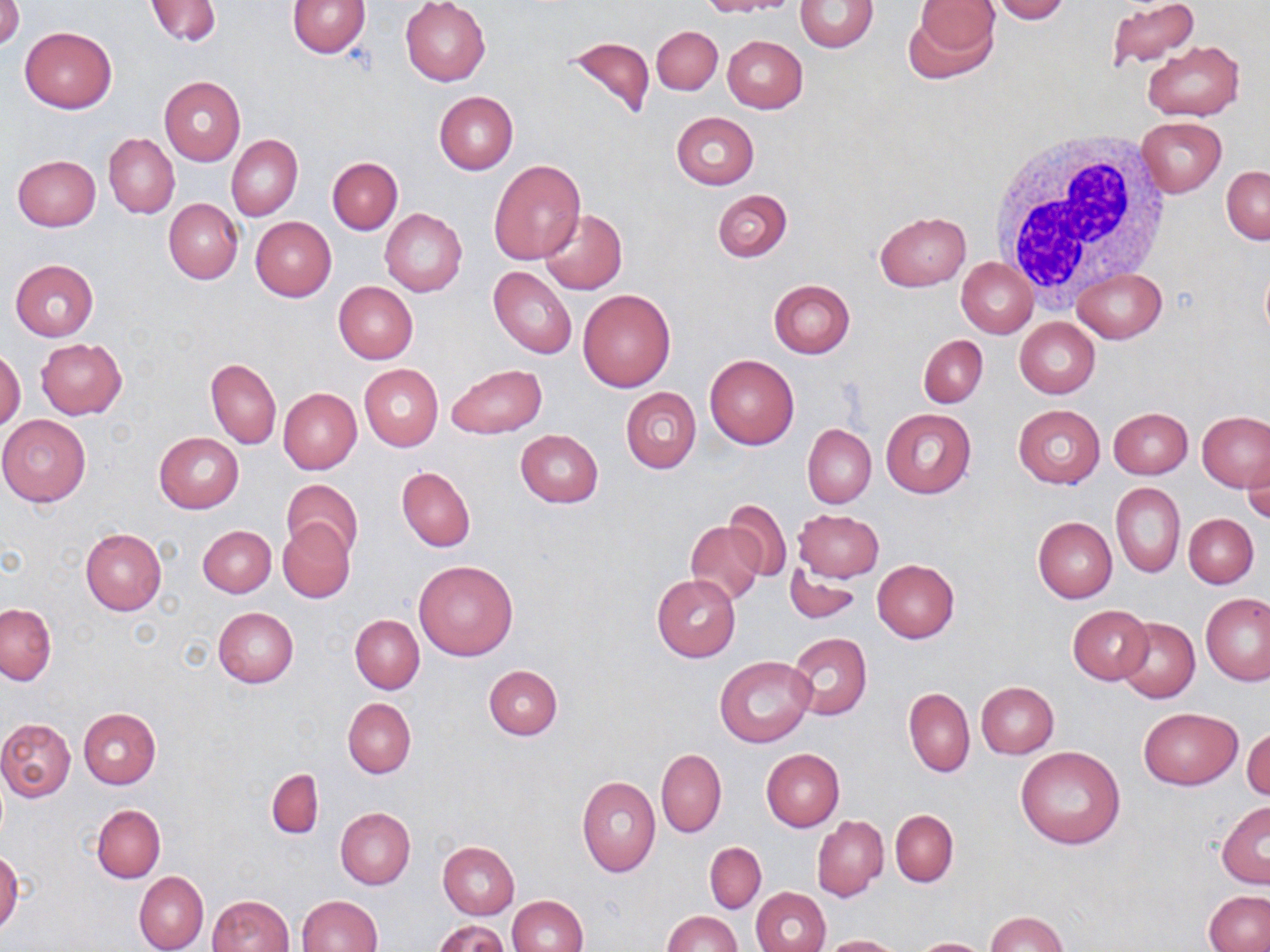
{
  "slide_level_diagnosis": "negative for blood parasites",
  "magnification": "1000x",
  "uninfected_red_blood_cell_locations": "approximate bounding boxes as (x1,y1)-(x2,y2) corner pairs in pixels: (1,0)-(23,48), (145,0)-(221,46), (288,0)-(369,57), (698,0)-(792,16), (989,0)-(1071,24), (1104,0)-(1200,70), (401,1)-(491,85), (795,1)-(878,53), (906,1)-(1000,81), (19,25)-(117,113), (652,26)-(723,94), (563,34)-(656,123), (723,35)-(808,113), (1143,41)-(1243,121), (159,76)-(245,166), (434,91)-(518,175), (671,112)-(759,189), (1135,116)-(1226,197), (104,133)-(179,218), (227,135)-(302,221), (12,155)-(102,230), (327,156)-(403,234), (488,160)-(585,264), (1222,166)-(1270,243), (713,189)-(792,262), (164,198)-(243,284), (380,209)-(467,296), (539,210)-(627,294), (875,212)-(970,290), (250,216)-(336,301), (955,258)-(1037,338), (1259,258)-(1270,346), (10,260)-(98,341), (488,266)-(577,358), (1071,267)-(1167,343), (768,279)-(855,357), (334,282)-(418,363), (577,288)-(677,392), (1015,317)-(1100,398), (918,335)-(987,408), (37,338)-(128,419), (0,349)-(25,431), (705,354)-(799,449), (207,359)-(281,449), (359,364)-(443,452), (445,364)-(546,438), (621,387)-(701,474), (279,388)-(361,473), (1014,404)-(1104,488), (880,407)-(976,500), (1108,407)-(1193,478), (1198,411)-(1268,491), (0,415)-(91,506), (803,424)-(875,508), (515,429)-(604,508), (154,431)-(244,513), (1242,451)-(1270,526), (396,466)-(475,553), (282,480)-(363,561), (1112,482)-(1185,577), (724,498)-(793,583), (793,510)-(884,582), (1184,514)-(1257,587), (1034,517)-(1116,602), (277,519)-(355,603), (686,522)-(764,606), (198,526)-(276,597), (81,528)-(167,615), (414,559)-(518,661), (872,559)-(959,642), (785,562)-(862,626), (653,574)-(740,661), (1202,593)-(1270,685), (1,604)-(55,685), (1067,606)-(1154,684), (214,607)-(299,687), (351,615)-(424,694), (1116,618)-(1199,703), (787,632)-(871,721), (716,655)-(814,748), (484,664)-(562,739), (976,682)-(1059,758), (904,688)-(974,776), (343,698)-(415,778), (79,708)-(160,789), (1139,708)-(1243,790), (0,718)-(75,801), (1244,728)-(1270,801), (1017,746)-(1126,850), (656,749)-(726,837), (762,749)-(843,831), (267,768)-(322,839), (577,775)-(660,876), (1217,801)-(1270,889), (92,804)-(165,882), (336,807)-(415,889), (890,809)-(958,886), (813,816)-(889,900), (438,842)-(519,918), (704,842)-(766,913), (0,851)-(23,934), (135,872)-(207,952), (751,887)-(830,952), (1204,890)-(1269,952), (207,895)-(293,952), (507,895)-(588,952), (298,896)-(382,952), (664,911)-(740,951), (986,911)-(1067,952), (435,920)-(511,952), (820,935)-(902,952), (909,938)-(995,951)",
  "modality": "light microscopy",
  "image_size": "1270×952 pixels",
  "field_of_view": "one of a larger specimen",
  "white_blood_cell_locations": "approximate bounding boxes as (x1,y1)-(x2,y2) corner pairs in pixels: (987,125)-(1170,305)",
  "preparation": "thin blood film",
  "stain": "May-Grünwald-Giemsa"
}